Assess the morphology of the red blood cells.
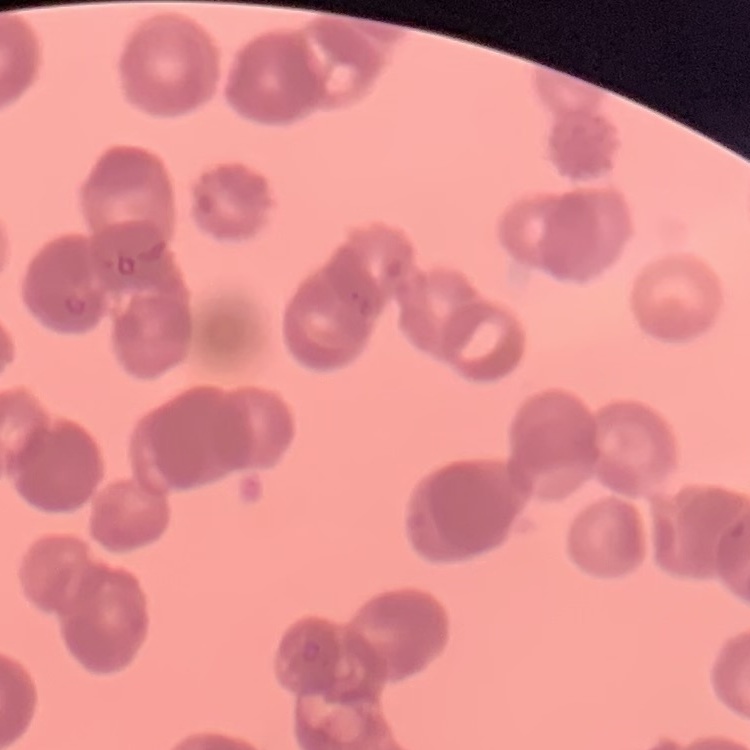
They show rouleaux formation.

preparation = thin blood smear
stain = Field's or Giemsa
image type = one tile cut from a larger photomicrograph